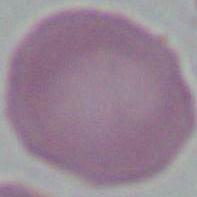
1000x magnification. Photomicrograph. A red blood cell is seen.